Assess this cell for malaria.
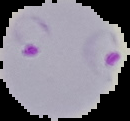

It is parasitized.

Summary:
  - Image size: 130×121 pixels
  - Preparation: thin blood smear
  - Image type: segmented cell region with the area outside set to black